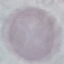

Summary:
  - Malaria status: uninfected
  - Stain: Giemsa
  - Capture: smartphone camera at the microscope eyepiece
  - Preparation: thin blood smear
  - Image type: automatically extracted cell patch, resized to 64 × 64 pixels